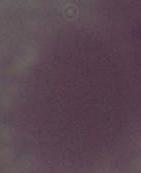

Summary:
  - Modality: micrograph
  - Magnification: 1000x
  - Identification: red blood cell